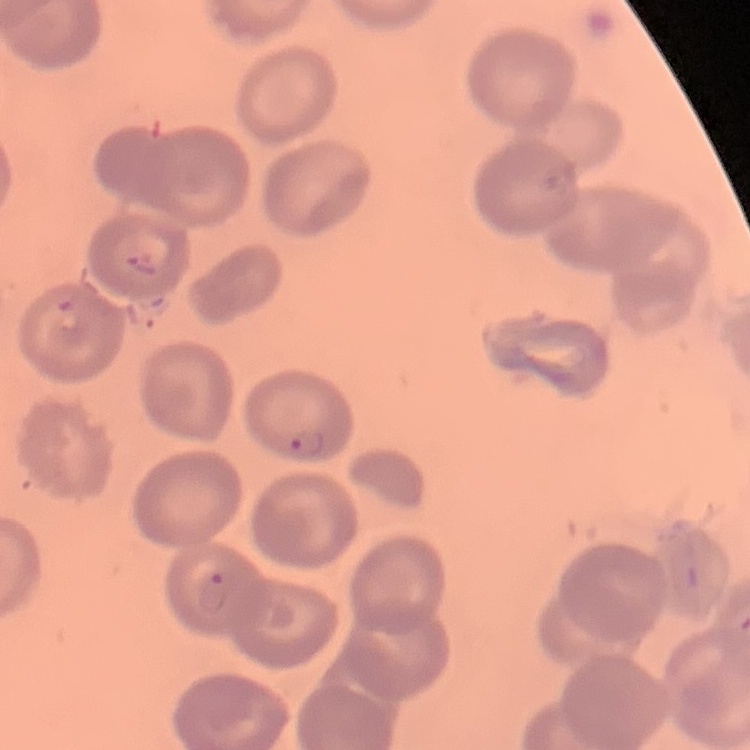
red blood cell morphology = no rouleaux formation
preparation = thin blood smear
image type = one tile cut from a larger photomicrograph
stain = Field's or Giemsa